Identify the cell.
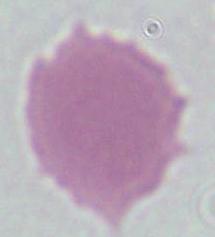

An erythrocyte.

1000x magnification. Micrograph.